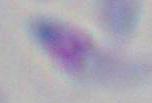
Photomicrograph. Captured at 1000x magnification. Toxoplasma gondii is shown.